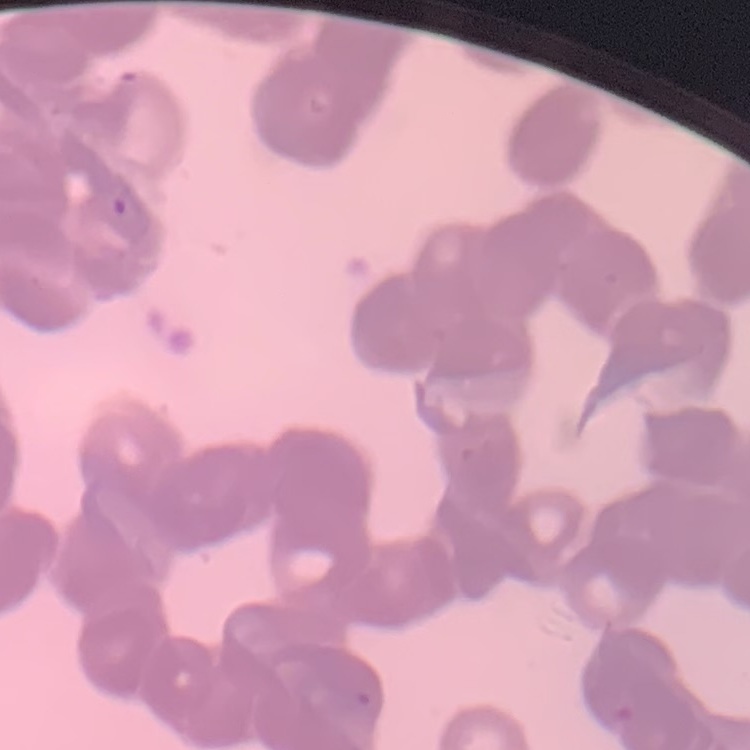

Summary:
  - Erythrocyte morphology: rouleaux formation
  - Preparation: thin blood film
  - Image type: one tile cut from a larger photomicrograph
  - Stain: Field's or Giemsa